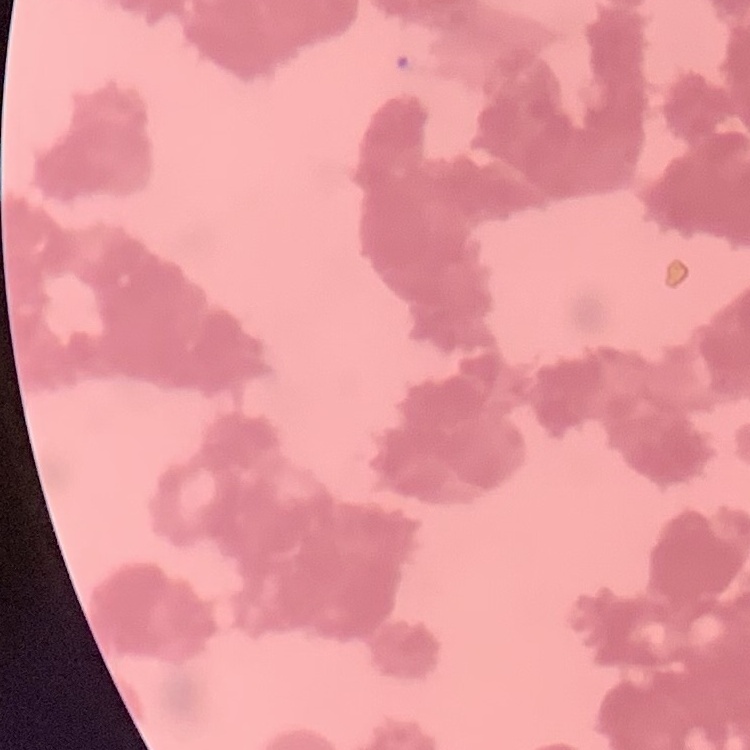
Summary:
  - Erythrocyte morphology: rouleaux formation
  - Image type: square crop of a larger photomicrograph
  - Preparation: thin blood film
  - Stain: Field's or Giemsa